Assess the morphology of the red blood cells.
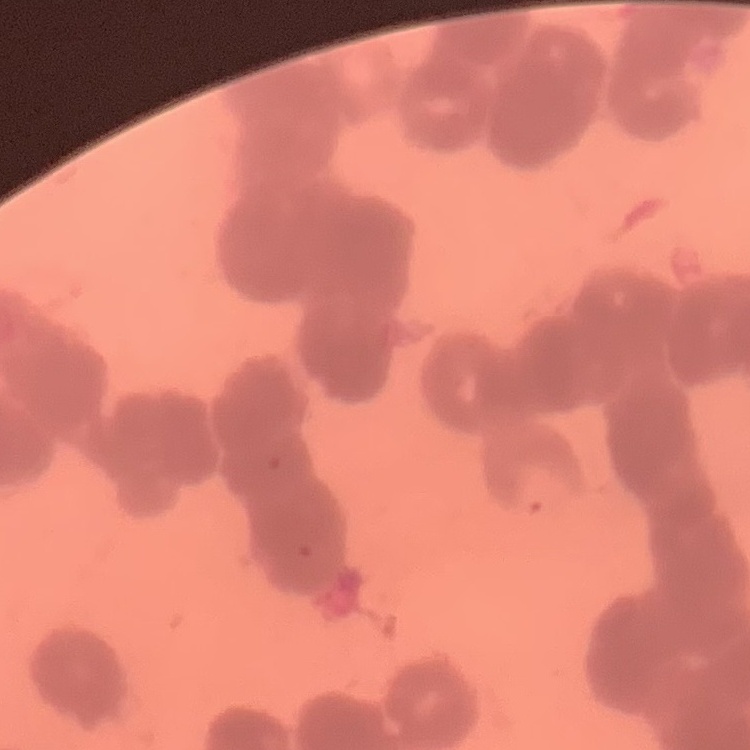
They show rouleaux formation.

Square crop of a larger photomicrograph. Stained with either Field's or Giemsa. Thin blood film.